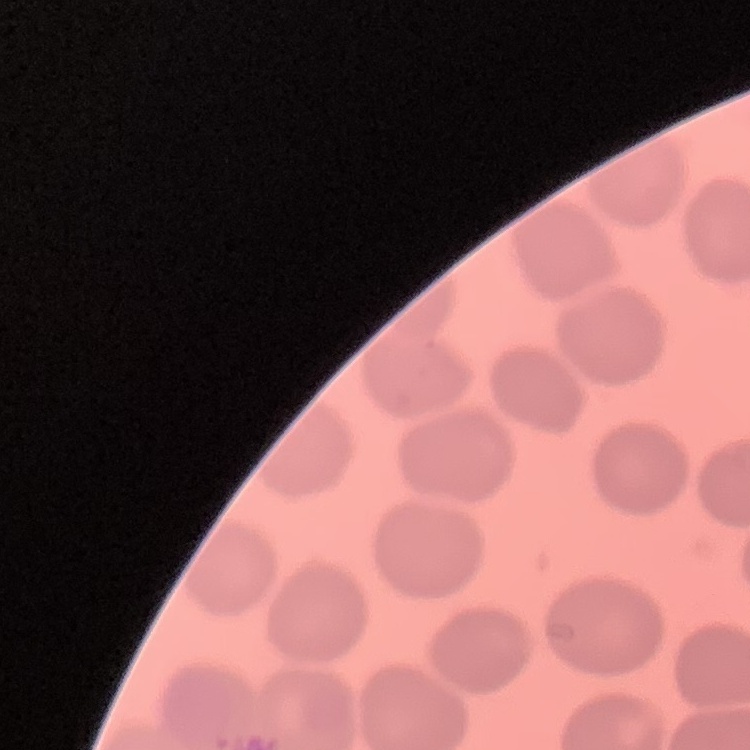

Summary:
  - Red blood cell morphology: no rouleaux formation
  - Image type: square crop of a larger photomicrograph
  - Stain: Field's or Giemsa
  - Preparation: thin peripheral smear